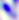
400x magnification. Toxoplasma gondii is seen. Photomicrograph.